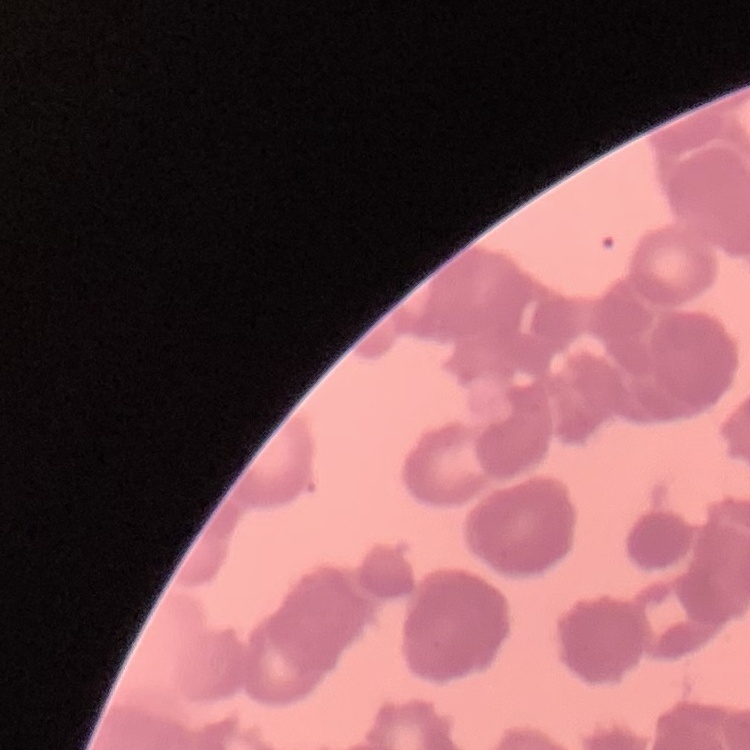

erythrocyte_morphology: rouleaux formation
image_type: one tile cut from a larger photomicrograph
stain: Field's or Giemsa
preparation: thin blood smear